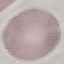
malaria status = uninfected
preparation = thin blood film
stain = Giemsa
capture = smartphone camera at the microscope eyepiece
image type = automatically extracted cell patch, resized to 64 × 64 pixels